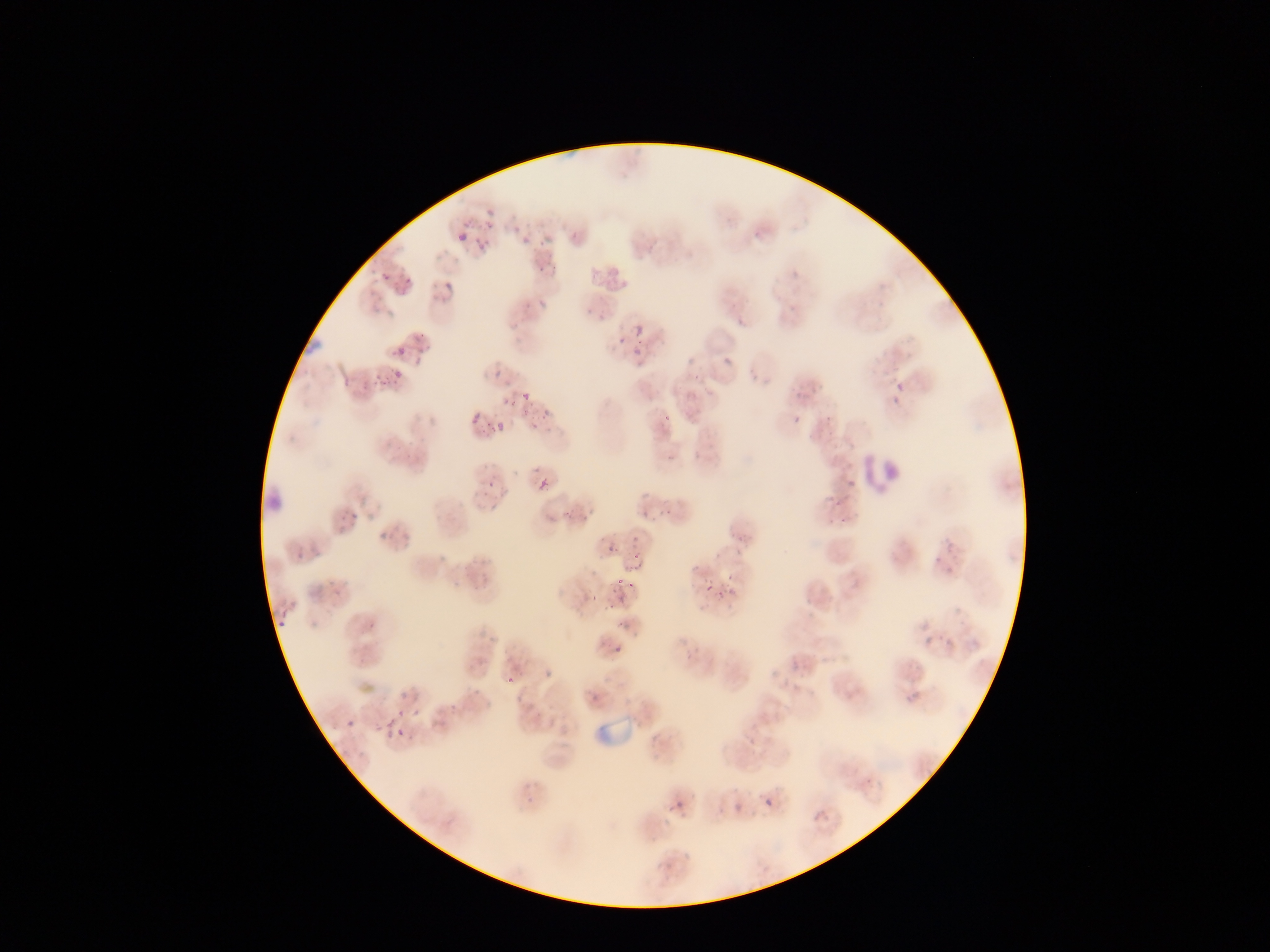

country = Ghana
preparation = thin blood film
leukocyte locations = approximate bounding boxes as [left, top, right, bottom] in pixels: [855, 452, 912, 509]
capture = mobile-phone photograph through a microscope
malaria parasite locations = approximate bounding boxes as [left, top, right, bottom] in pixels: [463, 211, 487, 222], [477, 224, 505, 258], [458, 232, 469, 244], [523, 234, 532, 245], [380, 272, 391, 282], [402, 277, 412, 287], [444, 281, 453, 289], [634, 323, 644, 334], [301, 333, 323, 353], [610, 335, 626, 354], [633, 338, 668, 369], [394, 347, 408, 360], [394, 370, 403, 380], [493, 370, 502, 379], [877, 377, 906, 410], [523, 393, 531, 401], [503, 397, 512, 405], [474, 412, 483, 422], [653, 412, 675, 430], [467, 414, 478, 424], [471, 414, 482, 426], [793, 415, 801, 425], [494, 422, 504, 432], [848, 478, 855, 488], [486, 479, 495, 488], [539, 479, 547, 489], [816, 494, 845, 522], [602, 537, 619, 552], [295, 550, 303, 559], [622, 564, 638, 582], [692, 566, 699, 574], [706, 584, 714, 592], [604, 594, 617, 609], [276, 616, 287, 629], [367, 621, 376, 631], [924, 635, 936, 645], [943, 636, 954, 648], [612, 645, 621, 654], [684, 652, 693, 660], [502, 666, 529, 690], [588, 691, 601, 705], [905, 691, 919, 705], [383, 710, 410, 744], [346, 720, 355, 729], [748, 737, 756, 745], [525, 795, 535, 805], [765, 799, 773, 806], [717, 808, 725, 817], [683, 851, 691, 859] | approximate [x, y] pixel centers of objects too small to bound: [727, 361]
field of view = single
image size = 1270×952 pixels